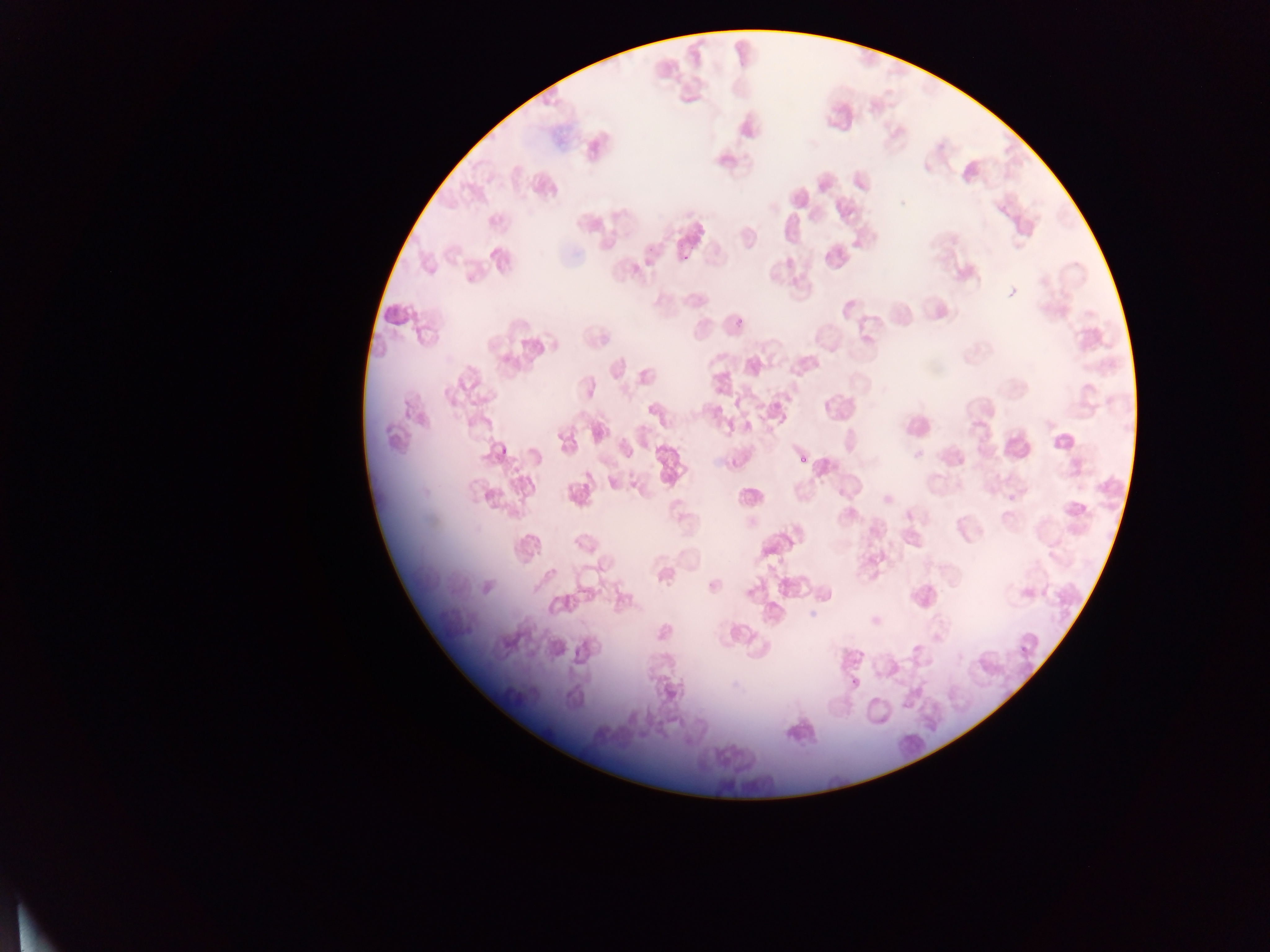

capture = mobile-phone photograph through a microscope
country = Ghana
malaria parasite locations = approximate bounding boxes as {left, top, right, bottom} in pixels: {574, 218, 584, 228}, {853, 240, 861, 248}, {730, 315, 745, 329}, {975, 420, 983, 427}, {498, 444, 511, 455}, {798, 451, 808, 469}, {584, 471, 593, 480}, {1019, 645, 1030, 654}
field of view = single
preparation = thin blood film
image size = 1270×952 pixels